Describe the morphology of the red blood cells.
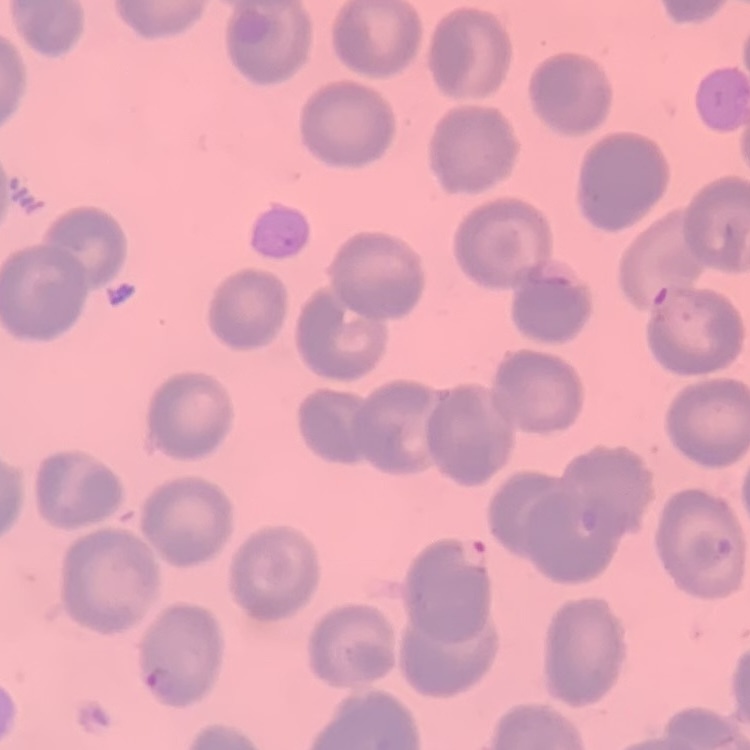
No rouleaux formation.

preparation = thin blood smear
image type = square crop of a larger photomicrograph
stain = Field's or Giemsa